Assess this cell for malaria.
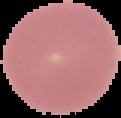
It is uninfected.

preparation = thin blood smear
image type = segmented cell region on a black background
image size = 121×118 pixels